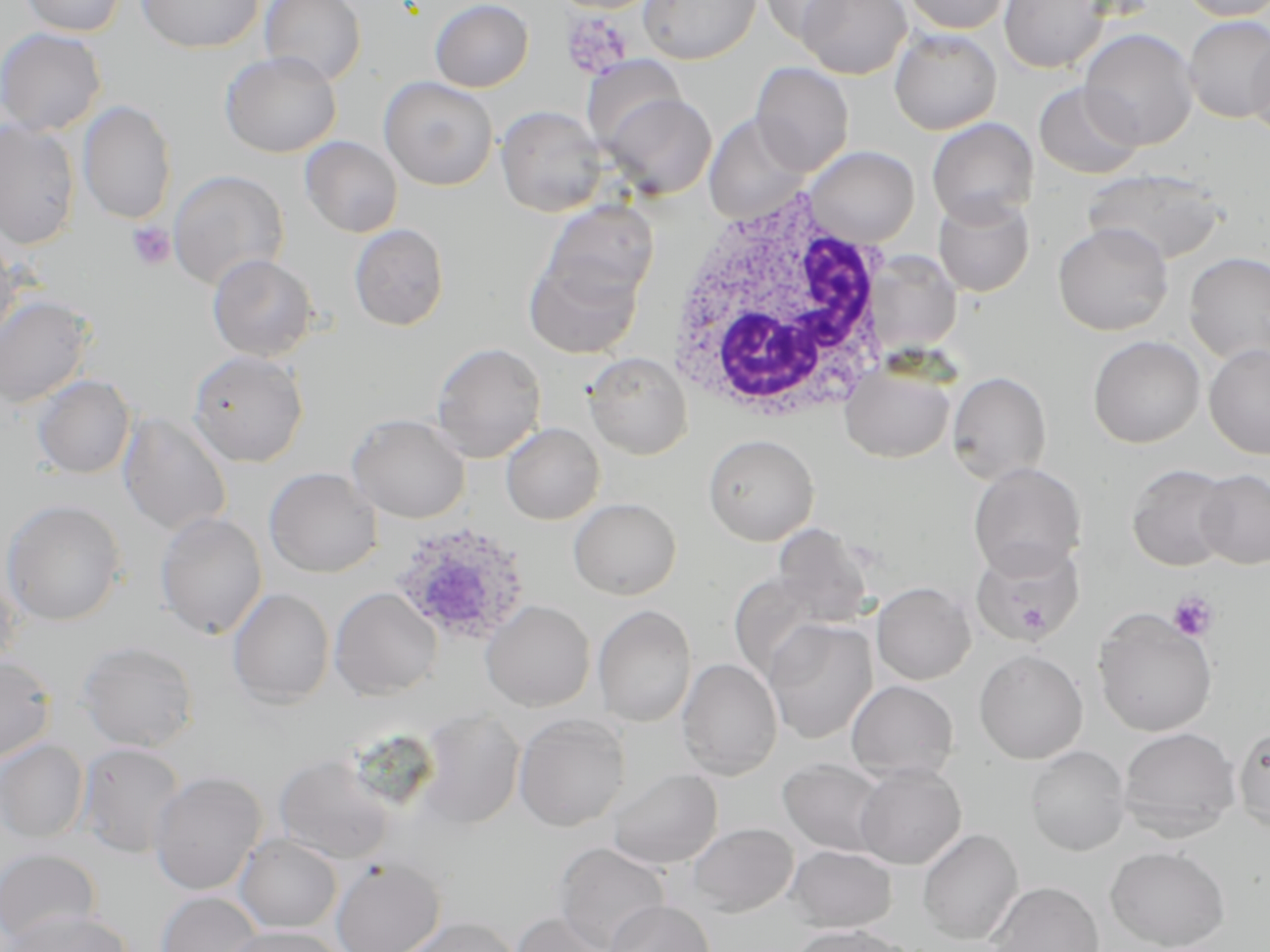
Approximate bounding boxes as (x1, y1, x2, y2) in pixels. Platelet locations: (562, 11, 635, 79), (126, 221, 176, 271), (1167, 591, 1219, 642). Uninfected red blood cell locations: (20, 0, 127, 37), (136, 0, 264, 53), (259, 0, 366, 87), (429, 0, 534, 92), (637, 0, 760, 64), (758, 0, 855, 42), (796, 0, 911, 79), (899, 0, 1013, 34), (998, 0, 1109, 74), (1179, 0, 1270, 21), (1183, 14, 1270, 123), (0, 27, 107, 136), (1078, 28, 1199, 150), (889, 29, 1002, 135), (1248, 35, 1270, 141), (220, 51, 342, 157), (579, 57, 685, 151), (751, 62, 854, 177), (378, 76, 498, 191), (1034, 82, 1144, 180), (602, 92, 717, 199), (78, 99, 176, 224), (496, 106, 606, 217), (703, 113, 812, 224), (927, 117, 1039, 226), (0, 121, 81, 249), (300, 136, 403, 238), (803, 145, 920, 247), (168, 169, 289, 291), (1082, 169, 1229, 265), (932, 194, 1035, 297), (543, 200, 660, 307), (1052, 222, 1174, 336), (349, 223, 449, 331), (0, 232, 23, 350), (1184, 252, 1270, 366), (523, 253, 643, 359), (207, 254, 319, 363), (870, 254, 965, 357), (0, 295, 94, 409), (1088, 335, 1205, 448), (430, 342, 547, 462), (1204, 344, 1270, 459), (188, 350, 308, 467), (583, 352, 692, 459), (840, 362, 955, 463), (946, 371, 1051, 483), (33, 375, 135, 479), (117, 412, 233, 537), (346, 414, 470, 523), (501, 422, 605, 524), (703, 434, 819, 546), (968, 462, 1086, 579), (1127, 464, 1234, 571), (264, 467, 382, 577), (1194, 469, 1270, 569), (568, 498, 681, 600), (0, 499, 127, 626), (154, 511, 267, 639), (772, 523, 875, 626), (971, 538, 1085, 646), (0, 570, 21, 677), (728, 572, 831, 683), (871, 581, 976, 685), (228, 587, 335, 708), (329, 587, 442, 700), (481, 600, 595, 711), (593, 604, 696, 728), (1093, 610, 1217, 737), (764, 618, 877, 744), (78, 640, 199, 752), (974, 649, 1088, 764), (0, 655, 56, 762), (676, 658, 782, 779), (846, 679, 959, 781), (414, 709, 526, 829), (513, 715, 630, 831), (1233, 724, 1270, 833), (1117, 726, 1241, 840), (0, 740, 89, 842), (76, 742, 186, 858), (1025, 746, 1131, 856), (275, 753, 395, 864), (777, 758, 890, 858), (853, 764, 966, 869), (607, 768, 723, 869), (148, 770, 267, 896), (685, 822, 799, 917), (917, 828, 1024, 945), (235, 834, 342, 933), (555, 842, 670, 952), (786, 845, 898, 932), (1105, 845, 1230, 951), (0, 847, 101, 949), (331, 858, 445, 952), (986, 882, 1104, 952), (156, 891, 264, 952), (605, 899, 714, 952), (5, 909, 132, 952), (512, 910, 615, 952), (398, 916, 522, 952), (789, 924, 910, 952), (223, 925, 347, 952). White blood cell locations: (666, 184, 895, 429). Plasmodium ovale-infected red blood cell locations: (389, 521, 532, 645). Slide-level diagnosis: Plasmodium ovale. Thin blood smear. One field of a larger specimen. May-Grünwald-Giemsa-stained preparation. 1000x magnification. Image is 1270×952 pixels. Optical microscopy.